Report the malaria status of this cell.
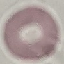

It is uninfected.

capture = smartphone camera at the microscope eyepiece
stain = Giemsa
preparation = thin smear
image type = cell patch, automatically extracted from a larger field of view and resized to 64 × 64 pixels